Give the extent of all white blood cells.
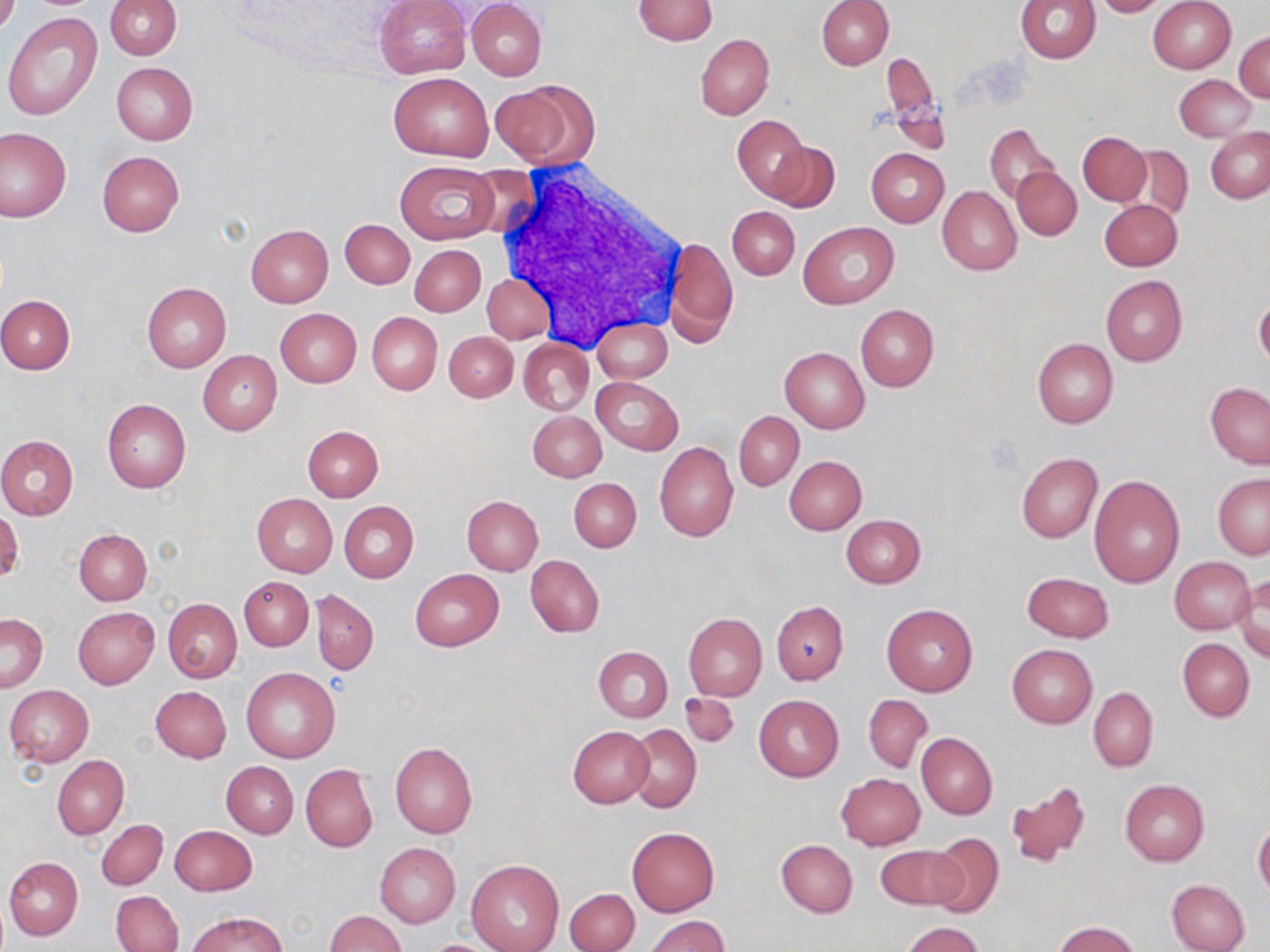
Approximate bounding boxes as [x1, y1, x2, y2] in pixels.
White blood cells: [483, 164, 682, 347].

{
  "slide_level_diagnosis": "negative for blood parasites",
  "magnification": "1000x",
  "uninfected_red_blood_cell_locations": "approximate bounding boxes as [x1, y1, x2, y2] in pixels: [0, 0, 19, 35], [105, 0, 181, 59], [375, 0, 470, 79], [466, 0, 546, 81], [633, 0, 717, 46], [816, 0, 893, 69], [1016, 0, 1100, 63], [1091, 0, 1171, 17], [1148, 1, 1236, 74], [5, 12, 105, 122], [1234, 32, 1270, 103], [695, 33, 774, 120], [880, 53, 940, 132], [111, 62, 198, 145], [388, 73, 492, 160], [1174, 74, 1256, 141], [490, 81, 594, 167], [732, 115, 809, 200], [985, 123, 1058, 205], [0, 126, 72, 223], [1206, 129, 1270, 203], [1078, 132, 1151, 206], [766, 140, 839, 213], [1125, 146, 1192, 222], [867, 148, 949, 227], [97, 150, 184, 236], [395, 160, 500, 245], [1011, 166, 1080, 240], [936, 185, 1022, 275], [1100, 199, 1182, 270], [728, 206, 799, 279], [339, 218, 414, 288], [798, 220, 899, 308], [246, 224, 333, 307], [666, 236, 737, 347], [410, 244, 486, 317], [482, 273, 556, 343], [1101, 274, 1187, 367], [141, 283, 231, 373], [0, 295, 74, 374], [1255, 296, 1270, 370], [855, 305, 939, 391], [275, 308, 361, 387], [367, 312, 442, 394], [591, 318, 671, 383], [444, 332, 517, 402], [519, 333, 669, 399], [1033, 338, 1118, 429], [519, 339, 594, 415], [780, 348, 869, 433], [198, 350, 282, 436], [592, 377, 683, 455], [1205, 382, 1270, 469], [102, 399, 191, 493], [733, 410, 803, 490], [528, 412, 606, 482], [303, 425, 382, 501], [0, 435, 78, 520], [654, 442, 738, 542], [1016, 452, 1102, 543], [784, 457, 866, 535], [1212, 473, 1270, 558], [1088, 474, 1185, 587], [569, 477, 641, 552], [251, 493, 337, 577], [462, 495, 543, 574], [338, 501, 418, 583], [0, 509, 21, 585], [842, 515, 925, 587], [75, 529, 152, 604], [526, 554, 605, 637], [1169, 556, 1254, 634], [411, 568, 504, 651], [1021, 573, 1113, 643], [238, 576, 313, 651], [1232, 576, 1269, 660], [311, 589, 379, 675], [163, 598, 241, 683], [771, 601, 848, 684], [881, 604, 978, 697], [73, 607, 159, 689], [683, 613, 766, 700], [1, 614, 49, 692], [1178, 638, 1254, 721], [1006, 645, 1096, 728], [594, 646, 672, 722], [242, 668, 340, 764], [5, 685, 94, 767], [150, 686, 232, 763], [1088, 688, 1157, 772], [680, 692, 738, 746], [862, 694, 932, 773], [754, 695, 842, 782], [627, 723, 702, 812], [567, 726, 653, 807], [917, 732, 997, 819], [390, 742, 477, 838], [52, 755, 128, 839], [221, 760, 298, 838], [301, 764, 378, 852], [836, 773, 926, 849], [1119, 778, 1209, 865], [1006, 782, 1089, 870], [97, 820, 167, 889], [1253, 821, 1270, 898], [169, 825, 257, 896], [626, 827, 719, 917], [926, 832, 1005, 918], [775, 839, 857, 917], [375, 843, 460, 927], [875, 844, 964, 911], [3, 856, 82, 941], [466, 859, 563, 952], [1167, 879, 1251, 952], [565, 885, 640, 952], [111, 890, 183, 952], [187, 911, 285, 951], [326, 911, 405, 952], [646, 916, 729, 952], [1054, 921, 1139, 952], [901, 922, 987, 952]",
  "field_of_view": "single",
  "preparation": "thin blood film",
  "image_size": "1270×952 pixels",
  "modality": "optical microscopy",
  "stain": "May-Grünwald-Giemsa"
}